Locate every blood parasite and identify its species.
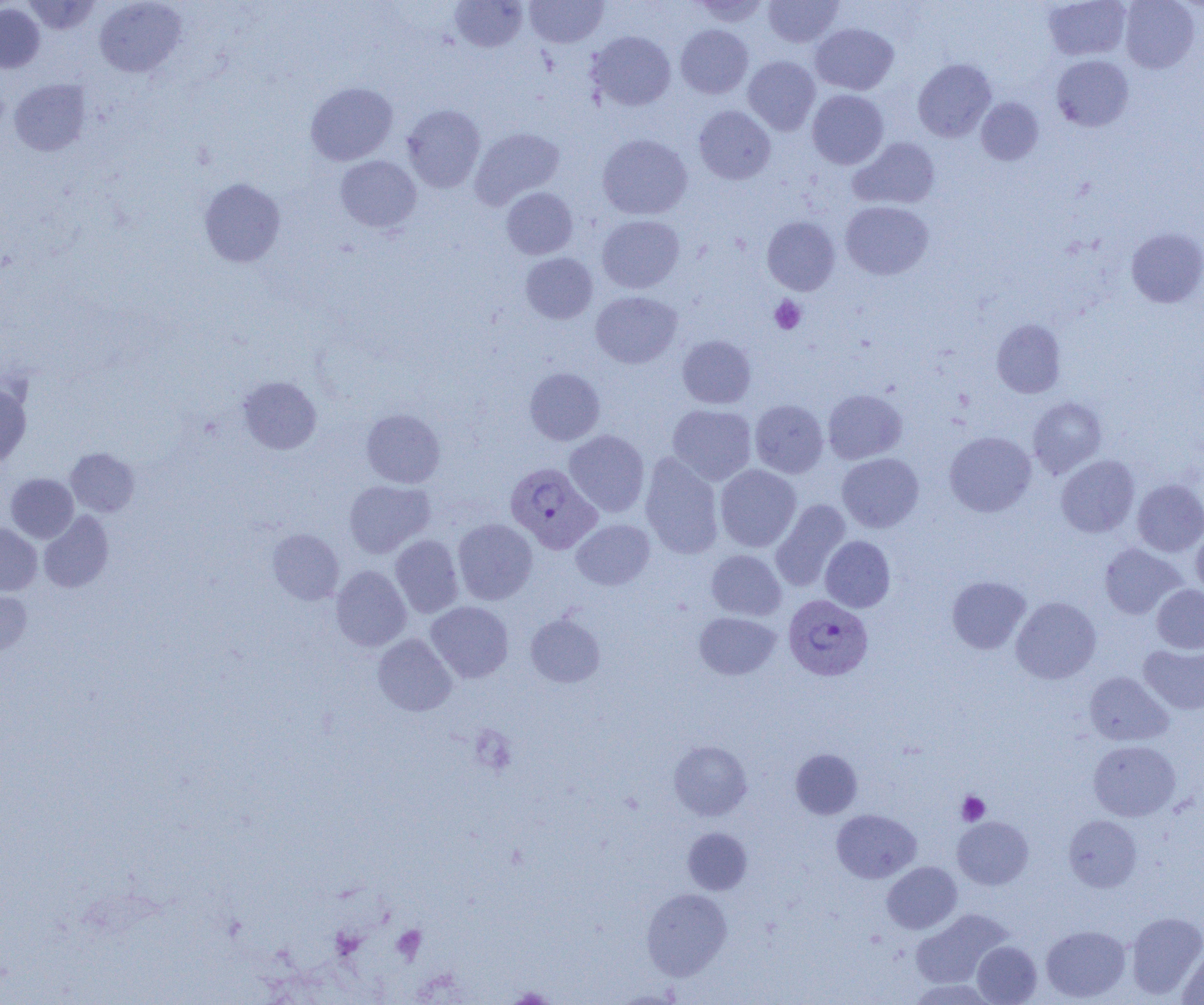
Approximate bounding boxes as (x1,y1)-(x2,y2) corner pairs in pixels.
Plasmodium vivax-infected red blood cells: (506,462)-(601,555), (784,594)-(873,681).
No Plasmodium falciparum, Plasmodium ovale, Plasmodium malariae, Babesia divergens, or Trypanosoma brucei observed.

Uninfected red blood cell locations: (23,0)-(101,34), (94,0)-(186,77), (449,0)-(527,52), (526,0)-(607,47), (1043,0)-(1131,61), (1120,0)-(1200,73), (691,1)-(771,27), (762,1)-(844,47), (0,3)-(44,73), (810,23)-(899,94), (676,24)-(753,98), (587,31)-(676,111), (1051,55)-(1134,131), (743,56)-(821,135), (912,58)-(996,142), (9,78)-(91,156), (305,81)-(398,165), (807,89)-(889,169), (976,98)-(1043,165), (402,105)-(485,192), (694,106)-(775,184), (470,127)-(564,209), (597,134)-(692,219), (850,137)-(940,209), (335,155)-(421,233), (199,178)-(285,267), (501,187)-(578,259), (840,201)-(933,280), (597,215)-(685,293), (762,216)-(840,295), (1126,227)-(1204,308), (521,253)-(598,324), (591,291)-(682,368), (992,319)-(1066,398), (678,335)-(756,408), (524,367)-(605,445), (237,376)-(321,454), (0,384)-(31,466), (823,389)-(907,464), (1027,396)-(1107,478), (750,400)-(828,478), (667,404)-(757,485), (361,409)-(445,488), (565,429)-(649,517), (944,431)-(1036,517), (66,448)-(139,517), (640,453)-(723,559), (837,453)-(923,533), (1056,455)-(1139,537), (715,464)-(801,551), (6,473)-(78,543), (1132,479)-(1204,556), (344,480)-(434,558), (771,499)-(851,591), (39,511)-(113,593), (453,518)-(537,605), (571,519)-(655,590), (0,523)-(42,595), (1191,528)-(1204,599), (267,529)-(344,604), (390,534)-(463,618), (820,536)-(895,612), (1099,543)-(1186,619), (706,550)-(786,621), (331,565)-(411,651), (947,576)-(1030,654), (1152,585)-(1204,654), (0,590)-(32,655), (1011,597)-(1101,684), (426,601)-(514,683), (694,612)-(781,679), (526,613)-(605,687), (373,634)-(456,715), (1139,643)-(1204,714), (1085,672)-(1173,746), (669,740)-(752,820), (1088,740)-(1181,820), (791,749)-(862,819), (831,809)-(921,883), (1063,815)-(1142,892), (952,816)-(1033,889), (683,827)-(752,894), (882,862)-(961,934), (641,888)-(732,980), (910,910)-(1010,988), (1127,911)-(1204,998), (1041,925)-(1130,1002), (972,941)-(1042,1004), (1177,945)-(1204,1005), (908,979)-(997,1004), (504,987)-(559,1004). Platelet locations: (770,295)-(806,334), (471,726)-(517,776), (956,791)-(990,825), (392,925)-(426,963), (504,987)-(559,1003). Slide-level diagnosis: Plasmodium vivax. Image is 1204×1005 pixels. Optical microscopy. Captured at 1000x magnification. One field of a larger specimen. Thin blood smear.